Name the cell type shown.
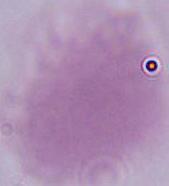
An erythrocyte.

magnification = 1000x
modality = photomicrograph